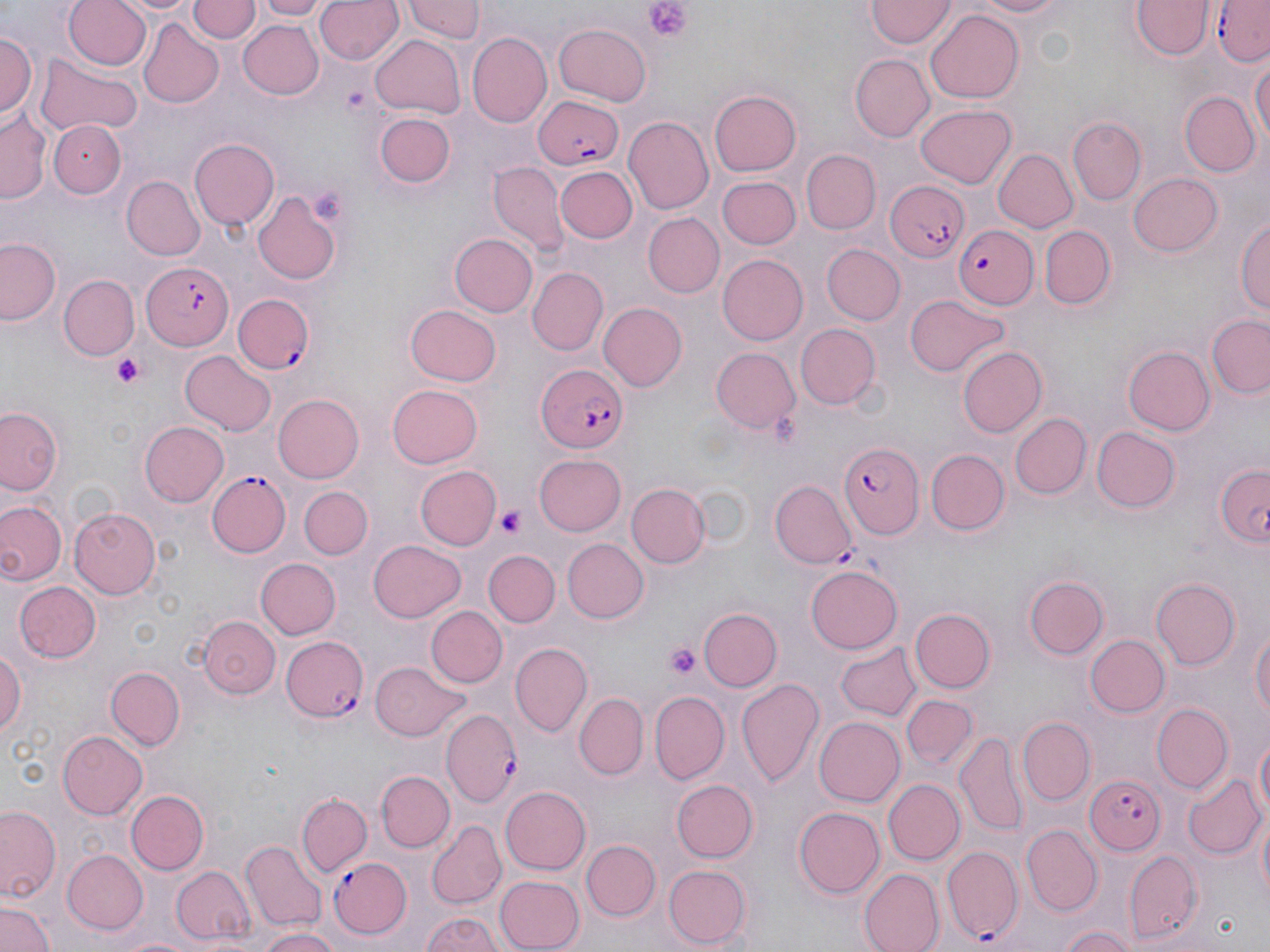
slide-level diagnosis = Plasmodium falciparum
stain = May-Grünwald-Giemsa
platelet locations = approximate bounding boxes as [x1, y1, x2, y2] in pixels: [641, 0, 695, 42], [113, 352, 150, 390], [498, 506, 526, 539], [667, 644, 701, 681]
magnification = 1000x
field of view = single
preparation = thin blood film
Plasmodium falciparum-infected red blood cell locations = approximate bounding boxes as [x1, y1, x2, y2] in pixels: [1212, 0, 1270, 65], [531, 96, 625, 168], [884, 180, 970, 263], [950, 225, 1038, 308], [141, 260, 235, 351], [235, 294, 315, 374], [535, 363, 631, 453], [837, 443, 924, 537], [206, 472, 291, 557], [280, 635, 369, 721], [441, 711, 522, 808], [1084, 773, 1164, 857], [942, 845, 1023, 941], [330, 855, 412, 939]
image size = 1270×952 pixels
uninfected red blood cell locations = approximate bounding boxes as [x1, y1, x2, y2] in pixels: [61, 0, 150, 72], [110, 0, 200, 17], [189, 0, 257, 43], [257, 0, 327, 21], [315, 0, 403, 66], [402, 0, 485, 42], [967, 0, 1075, 19], [867, 1, 955, 48], [1130, 2, 1212, 61], [926, 8, 1024, 102], [139, 18, 225, 108], [236, 19, 322, 101], [553, 22, 651, 106], [1, 29, 37, 123], [469, 31, 551, 125], [369, 34, 468, 119], [34, 52, 141, 137], [1251, 53, 1269, 156], [850, 54, 933, 142], [708, 89, 803, 176], [1179, 90, 1258, 178], [915, 104, 1019, 187], [1, 112, 48, 202], [378, 115, 453, 186], [625, 116, 713, 213], [1069, 118, 1145, 202], [48, 121, 129, 199], [189, 138, 279, 230], [995, 148, 1079, 233], [803, 150, 880, 233], [488, 159, 569, 257], [555, 165, 637, 242], [1128, 170, 1223, 256], [718, 176, 798, 248], [121, 177, 205, 260], [252, 190, 340, 285], [1235, 212, 1270, 320], [644, 213, 724, 297], [1040, 223, 1116, 310], [451, 232, 537, 316], [1, 237, 61, 326], [821, 244, 905, 326], [718, 254, 808, 344], [528, 266, 608, 356], [60, 275, 139, 360], [904, 293, 1012, 379], [597, 302, 685, 392], [404, 303, 502, 386], [1208, 314, 1270, 400], [794, 324, 878, 408], [958, 346, 1047, 438], [1122, 346, 1215, 436], [710, 348, 800, 435], [181, 350, 276, 436], [386, 383, 482, 469], [272, 392, 363, 483], [0, 405, 65, 496], [1012, 413, 1091, 498], [140, 421, 228, 506], [1090, 426, 1180, 513], [925, 450, 1006, 535], [535, 453, 627, 535], [1216, 465, 1269, 547], [415, 466, 501, 550], [771, 482, 854, 567], [300, 484, 375, 559], [628, 485, 709, 568], [0, 499, 65, 588], [70, 508, 161, 598], [564, 538, 650, 623], [368, 539, 467, 624], [483, 549, 559, 627], [255, 557, 341, 639], [806, 566, 902, 653], [1021, 570, 1111, 661], [1153, 578, 1240, 668], [13, 580, 101, 663], [425, 605, 508, 689], [911, 606, 995, 692], [697, 609, 781, 693], [201, 615, 280, 696], [1247, 619, 1270, 729], [1086, 636, 1169, 716], [835, 640, 922, 722], [510, 643, 590, 737], [0, 647, 26, 742], [370, 662, 469, 741], [106, 667, 184, 748], [737, 677, 824, 792], [650, 691, 729, 782], [574, 693, 647, 779], [902, 693, 977, 771], [1152, 704, 1232, 793], [815, 715, 905, 806], [1018, 718, 1094, 803], [1253, 729, 1269, 827], [57, 730, 148, 820], [958, 735, 1027, 833], [378, 770, 452, 851], [1185, 773, 1265, 859], [672, 780, 758, 861], [874, 780, 954, 945], [883, 780, 965, 864], [501, 785, 591, 873], [126, 790, 209, 874], [298, 794, 371, 877], [1, 802, 62, 903], [1253, 802, 1269, 909], [793, 806, 885, 898], [428, 822, 505, 907], [1023, 825, 1100, 913], [583, 840, 659, 920], [241, 842, 326, 931], [62, 851, 147, 935], [1124, 851, 1203, 945], [662, 864, 749, 948], [171, 865, 255, 945], [859, 869, 943, 952], [491, 874, 583, 952], [1, 899, 53, 952], [420, 912, 504, 952], [1055, 925, 1137, 952], [253, 927, 342, 952], [112, 934, 198, 952]
modality = optical microscopy